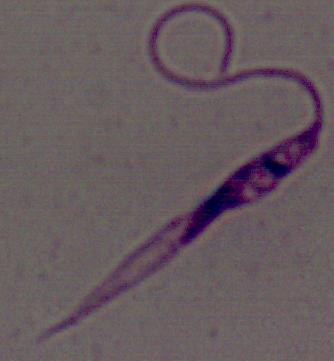

magnification: 1000x
identification: Leishmania
modality: micrograph